State which cell type is depicted.
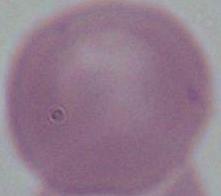

An erythrocyte.

Micrograph. Captured at 1000x magnification.